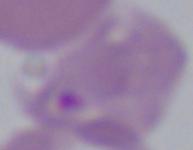 Micrograph. Captured at 1000x magnification. A Babesia parasite is seen.